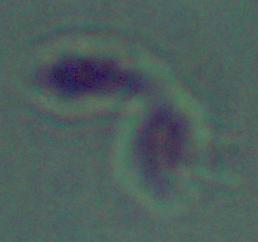
Photomicrograph. 1000x magnification. A Leishmania parasite is seen.